Report the malaria status of this cell.
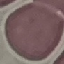

Uninfected.

stain = Giemsa
capture = smartphone camera at the microscope eyepiece
image type = cell patch, automatically extracted from a larger field of view and resized to 64 × 64 pixels
preparation = thin blood smear